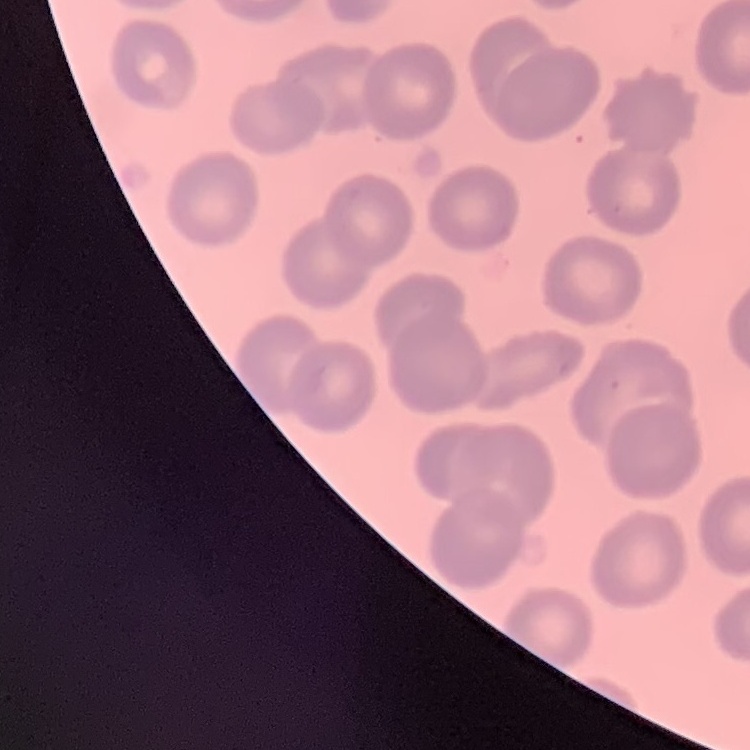 The erythrocytes show no rouleaux formation. Field's or Giemsa stain. Square crop of a larger photomicrograph. Thin blood smear.